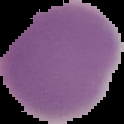

Summary:
  - Image type: cell region segmented out of the field of view; surrounding area masked to black
  - Preparation: thin blood film
  - Image size: 124×124 pixels
  - Malaria status: uninfected